State the preparation type.
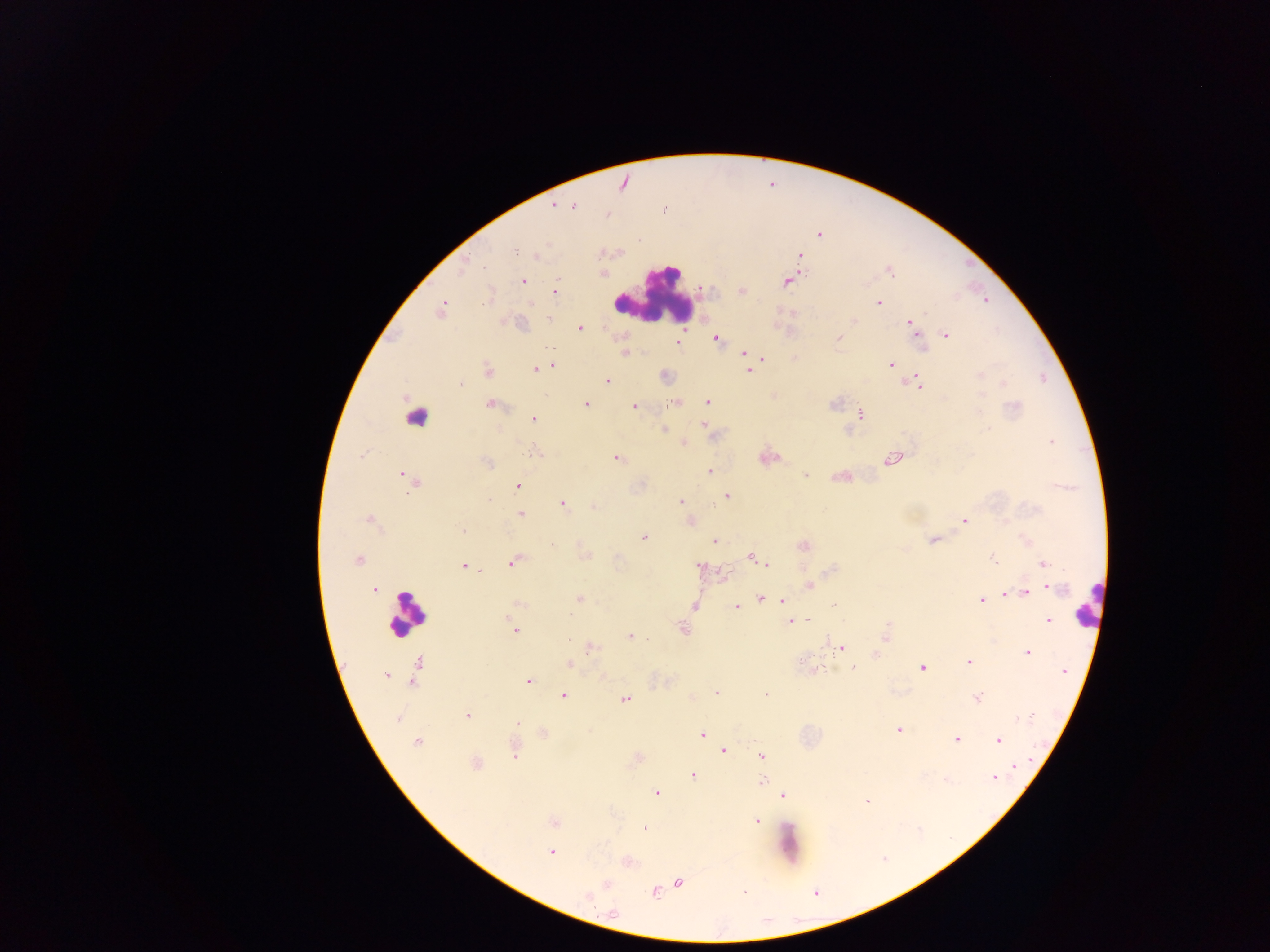
Thick blood smear.

leukocyte locations = approximate centers as [x, y] in pixels: [654, 295], [415, 411], [1087, 604], [407, 615]
field of view = single
Plasmodium parasite locations = approximate centers as [x, y] in pixels: [623, 183], [553, 205], [574, 206], [607, 215], [820, 236], [515, 252], [801, 255], [537, 257], [465, 268], [890, 272], [602, 273], [523, 281], [787, 282], [702, 290], [742, 291], [554, 292], [485, 301], [879, 303], [529, 304], [441, 310], [549, 319], [853, 321], [910, 323], [581, 328], [946, 335], [839, 338], [716, 339], [677, 342], [918, 342], [549, 348], [743, 354], [763, 358], [891, 364], [551, 365], [534, 369], [748, 370], [488, 371], [980, 374], [607, 381], [918, 383], [461, 384], [674, 402], [708, 402], [489, 404], [586, 404], [833, 404], [635, 406], [1015, 407], [861, 415], [533, 419], [702, 425], [664, 429], [987, 429], [1051, 442], [684, 443], [534, 452], [616, 459], [893, 459], [486, 462], [710, 472], [805, 476], [405, 477], [411, 483], [518, 486], [728, 496], [489, 500], [682, 501], [563, 504], [594, 507], [518, 509], [521, 514], [964, 520], [369, 521], [462, 530], [644, 537], [932, 540], [715, 541], [552, 546], [803, 546], [586, 556], [753, 558], [992, 558], [358, 560], [762, 562], [512, 563], [1044, 564], [463, 566], [699, 566], [725, 576], [808, 585], [375, 589], [1054, 589], [1026, 593], [1009, 594], [760, 598], [579, 599], [982, 600], [782, 601], [520, 604], [695, 605], [833, 606], [735, 607], [570, 616], [808, 619], [1048, 620], [791, 621], [683, 629], [515, 631], [886, 635], [630, 636], [570, 640], [842, 647], [591, 648], [1027, 653], [875, 655], [969, 661], [417, 663], [568, 664], [853, 668], [923, 668], [1064, 672], [386, 676], [528, 681], [716, 692], [766, 695], [563, 696], [976, 698], [625, 699], [467, 715], [397, 718], [1029, 719], [516, 723], [898, 730], [543, 734], [702, 735], [956, 739], [999, 741], [416, 742], [724, 751], [515, 752], [762, 756], [475, 764], [1014, 766], [692, 775], [993, 778], [761, 781], [657, 793], [783, 795], [867, 802], [553, 822], [756, 822], [644, 828], [551, 852], [679, 882], [607, 884], [654, 893], [744, 893], [588, 896], [613, 913]
capture = mobile-phone photograph through a microscope
image size = 1270×952 pixels
country = Ghana